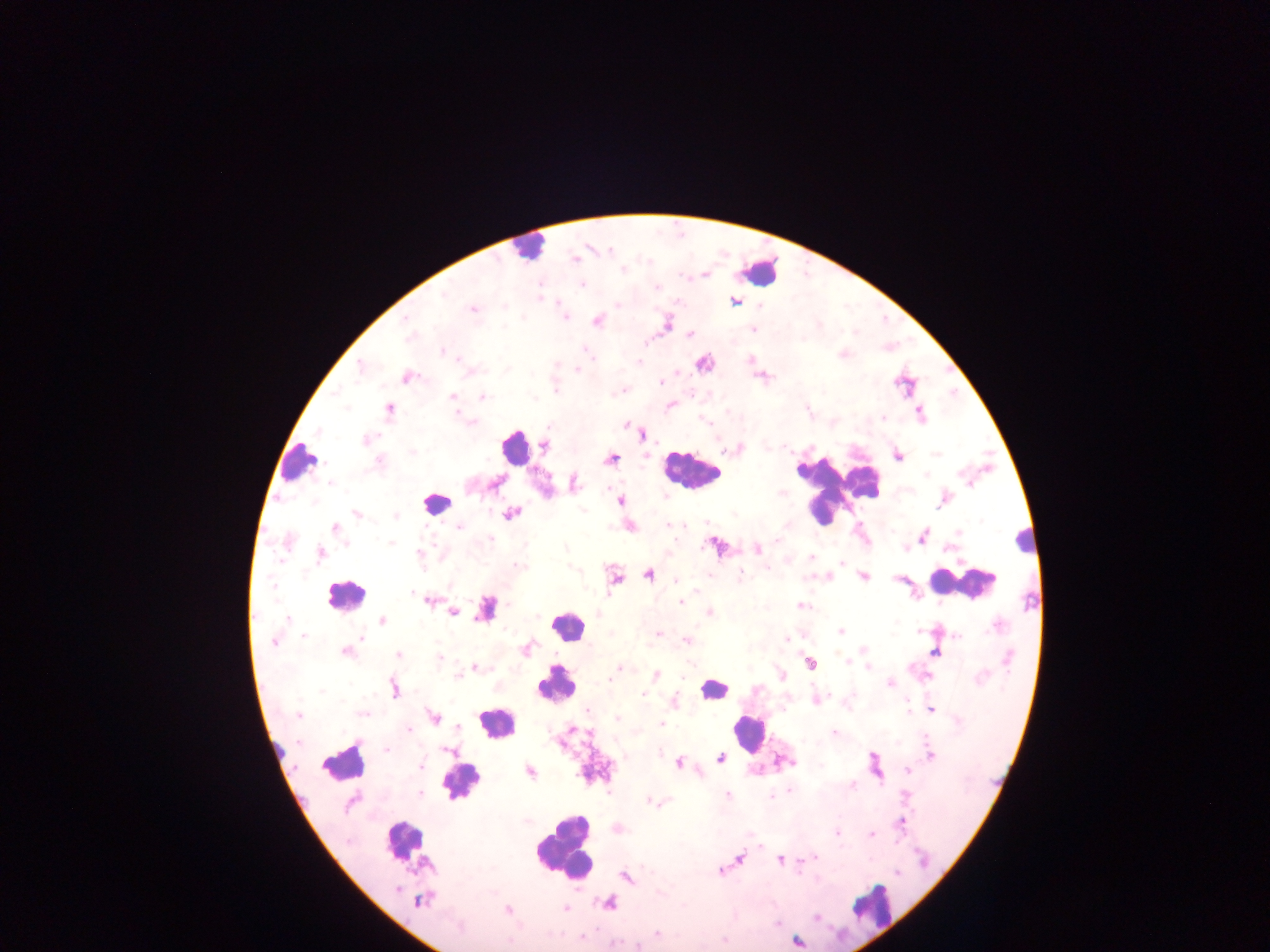
preparation = thick blood film
image size = 1270×952 pixels
country = Ghana
Plasmodium parasite locations = approximate centers as (x, y) in pixels: (576, 258), (623, 270), (583, 285), (657, 287), (444, 294), (735, 301), (617, 305), (473, 309), (406, 318), (566, 318), (597, 322), (752, 329), (408, 334), (690, 334), (585, 350), (443, 352), (588, 353), (640, 363), (360, 368), (577, 369), (407, 378), (661, 381), (556, 391), (453, 397), (482, 397), (670, 406), (346, 407), (389, 410), (921, 414), (883, 418), (472, 422), (626, 425), (367, 440), (544, 447), (739, 448), (413, 452), (898, 456), (611, 459), (379, 462), (925, 474), (330, 483), (495, 483), (573, 483), (620, 501), (582, 509), (357, 514), (512, 514), (396, 516), (672, 524), (681, 525), (459, 527), (335, 529), (958, 533), (923, 536), (490, 539), (777, 541), (287, 543), (391, 543), (346, 544), (566, 548), (757, 550), (321, 554), (421, 554), (811, 557), (841, 563), (518, 565), (768, 569), (740, 574), (649, 575), (863, 576), (615, 578), (676, 581), (413, 593), (430, 601), (680, 602), (801, 606), (485, 608), (452, 612), (710, 613), (288, 619), (382, 621), (841, 631), (918, 631), (658, 634), (304, 636), (958, 636), (361, 638), (787, 639), (688, 641), (273, 643), (863, 649), (346, 652), (934, 653), (398, 654), (438, 659), (848, 662), (810, 664), (475, 667), (868, 667), (619, 669), (656, 675), (458, 676), (609, 680), (891, 683), (394, 689), (322, 691), (644, 695), (932, 709), (588, 711), (363, 714), (298, 715), (433, 717), (617, 718), (661, 724), (409, 730), (834, 732), (387, 750), (450, 752), (930, 754), (719, 758), (679, 763), (420, 767), (530, 771), (908, 771), (853, 786), (789, 791), (420, 793), (727, 794), (772, 795), (906, 795), (649, 801), (350, 803), (901, 823), (837, 833), (871, 834), (760, 846), (815, 857), (739, 858), (781, 860), (719, 871), (625, 877), (420, 901), (566, 909), (508, 910), (816, 918), (658, 934), (582, 937), (798, 941), (637, 946)
leukocyte locations = approximate centers as (x, y) in pixels: (527, 248), (762, 271), (514, 446), (298, 462), (693, 471), (832, 490), (437, 503), (1024, 538), (961, 583), (345, 596), (568, 626), (555, 686), (713, 689), (495, 723), (747, 732), (276, 750), (346, 763), (462, 784), (402, 840), (563, 850), (878, 907)
capture = mobile-phone photograph through a microscope
field of view = single